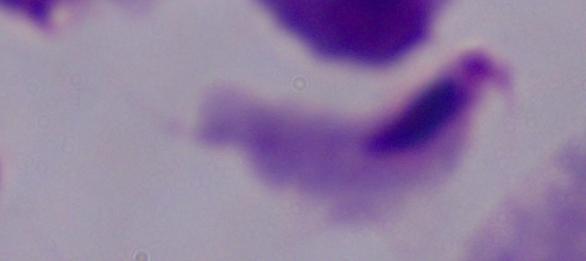

magnification: 1000x
identification: trichomonad
modality: micrograph